Outline each Trypanosoma brucei.
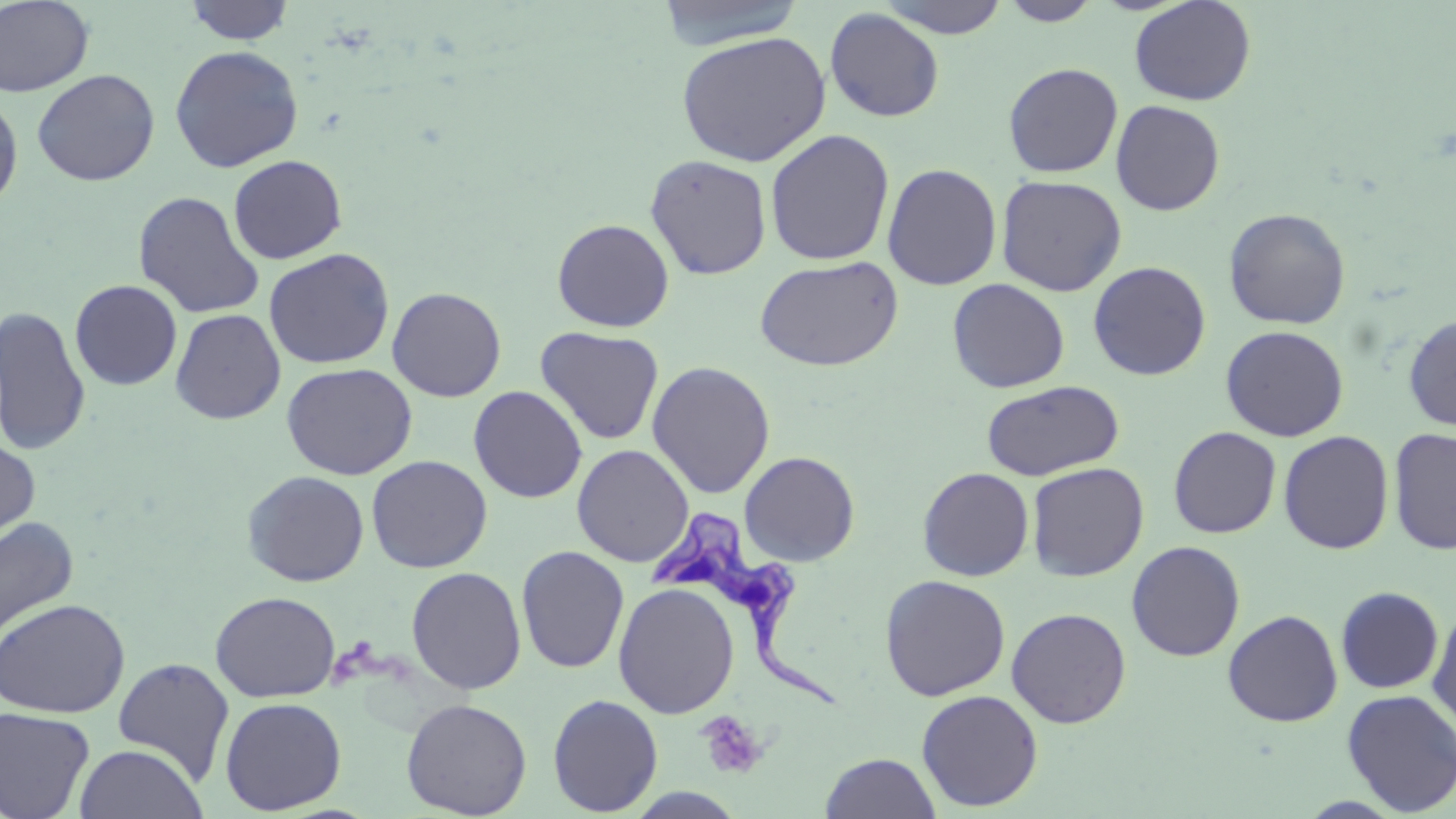

Approximate bounding boxes as named x1/y1/x2/y2 corners in pixels.
Trypanosoma brucei: (x1=647, y1=512, x2=839, y2=713).

Platelet locations: (x1=696, y1=711, x2=770, y2=781). Uninfected red blood cell locations: (x1=0, y1=0, x2=95, y2=98), (x1=653, y1=0, x2=808, y2=49), (x1=877, y1=0, x2=1011, y2=38), (x1=182, y1=1, x2=296, y2=45), (x1=998, y1=1, x2=1104, y2=26), (x1=1129, y1=1, x2=1257, y2=106), (x1=824, y1=7, x2=945, y2=123), (x1=676, y1=31, x2=831, y2=167), (x1=169, y1=44, x2=304, y2=172), (x1=1003, y1=62, x2=1123, y2=178), (x1=31, y1=68, x2=160, y2=186), (x1=0, y1=91, x2=23, y2=213), (x1=1111, y1=99, x2=1225, y2=216), (x1=765, y1=129, x2=895, y2=266), (x1=644, y1=153, x2=772, y2=280), (x1=228, y1=154, x2=348, y2=264), (x1=882, y1=163, x2=1002, y2=290), (x1=996, y1=175, x2=1127, y2=296), (x1=133, y1=190, x2=265, y2=319), (x1=1223, y1=207, x2=1351, y2=329), (x1=552, y1=218, x2=675, y2=332), (x1=263, y1=247, x2=396, y2=369), (x1=754, y1=255, x2=904, y2=372), (x1=1088, y1=261, x2=1211, y2=380), (x1=947, y1=278, x2=1070, y2=393), (x1=70, y1=279, x2=183, y2=390), (x1=387, y1=286, x2=507, y2=401), (x1=0, y1=305, x2=92, y2=456), (x1=170, y1=307, x2=286, y2=424), (x1=1402, y1=314, x2=1456, y2=432), (x1=1220, y1=325, x2=1349, y2=442), (x1=535, y1=326, x2=664, y2=446), (x1=647, y1=361, x2=776, y2=499), (x1=281, y1=362, x2=418, y2=480), (x1=980, y1=379, x2=1124, y2=481), (x1=468, y1=385, x2=588, y2=503), (x1=1168, y1=426, x2=1281, y2=538), (x1=1388, y1=427, x2=1456, y2=555), (x1=1278, y1=430, x2=1394, y2=555), (x1=0, y1=435, x2=41, y2=549), (x1=572, y1=444, x2=694, y2=567), (x1=739, y1=451, x2=860, y2=567), (x1=366, y1=454, x2=492, y2=573), (x1=1026, y1=461, x2=1149, y2=581), (x1=917, y1=467, x2=1034, y2=581), (x1=242, y1=470, x2=370, y2=587), (x1=0, y1=516, x2=79, y2=644), (x1=1126, y1=540, x2=1246, y2=661), (x1=516, y1=545, x2=630, y2=674), (x1=406, y1=566, x2=527, y2=694), (x1=880, y1=574, x2=1011, y2=701), (x1=613, y1=583, x2=740, y2=718), (x1=1335, y1=586, x2=1444, y2=694), (x1=210, y1=591, x2=340, y2=702), (x1=0, y1=598, x2=130, y2=718), (x1=1427, y1=604, x2=1456, y2=734), (x1=1006, y1=607, x2=1132, y2=728), (x1=1222, y1=609, x2=1343, y2=727), (x1=112, y1=658, x2=236, y2=786), (x1=1341, y1=688, x2=1456, y2=816), (x1=916, y1=689, x2=1044, y2=812), (x1=547, y1=693, x2=663, y2=816), (x1=220, y1=696, x2=347, y2=815), (x1=401, y1=698, x2=532, y2=818), (x1=0, y1=706, x2=95, y2=819), (x1=74, y1=743, x2=208, y2=819), (x1=819, y1=752, x2=942, y2=818). Slide-level diagnosis: Trypanosoma brucei. Light microscopy. Image is 1456×819 pixels. 1000x magnification. May-Grünwald-Giemsa-stained preparation. One field of a larger specimen. Thin blood film.